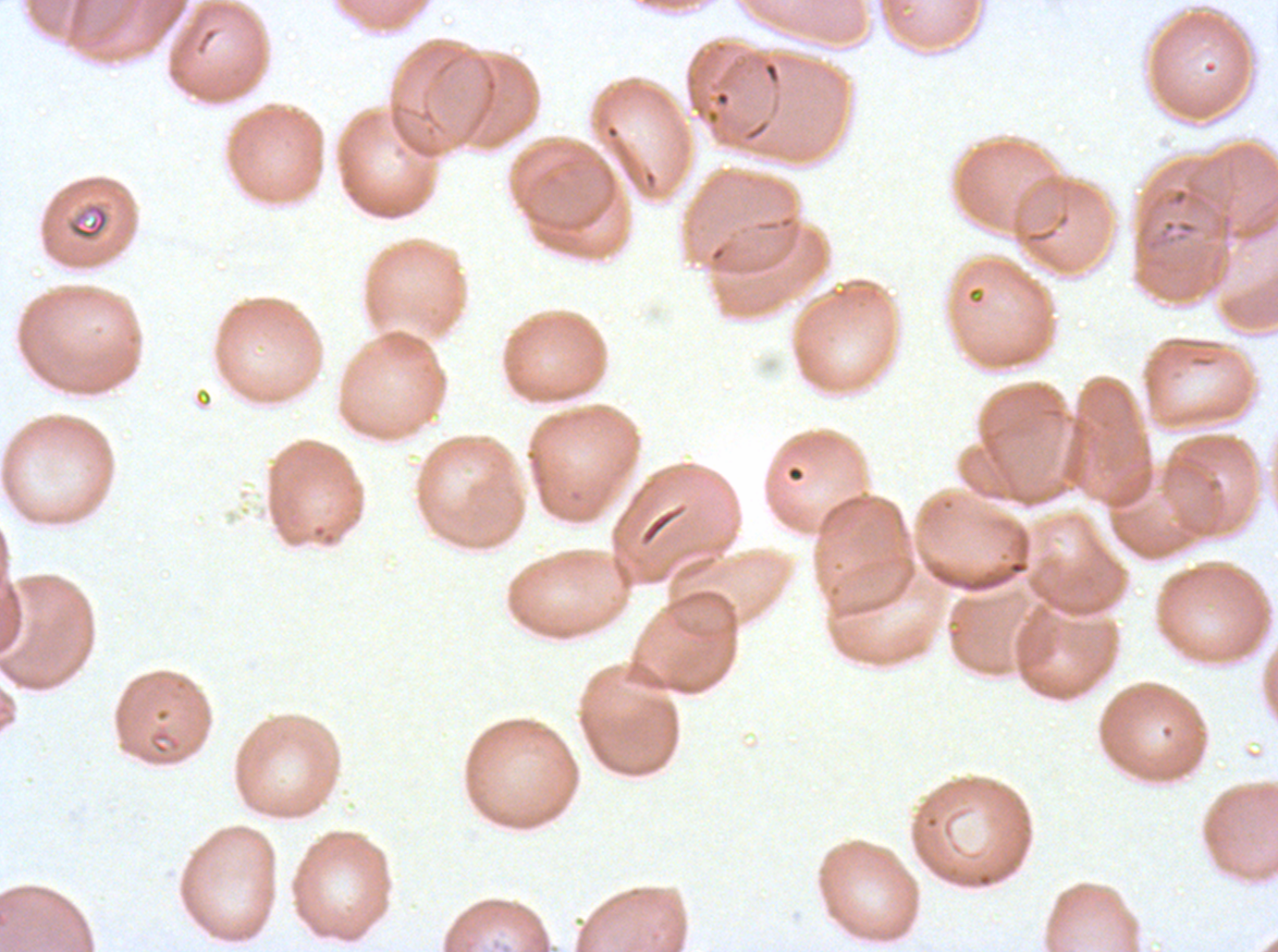
field_of_view: one sub-image of a larger composite
specimen: P. falciparum from a patient in The Gambia, cultured ex vivo for 24 to 48 hours
preparation: thin blood smear
stain: Giemsa
ring_locations: 'approximate bounding boxes as {x1, y1, x2, y2} in pixels: {1146, 217, 1199, 250}'
debris_locations: 'approximate bounding boxes as {x1, y1, x2, y2} in pixels: {67, 202, 109, 241}'
image_size: 1278×952 pixels